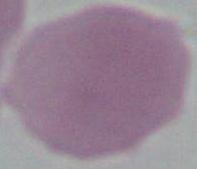
modality = photomicrograph
magnification = 1000x
identification = red blood cell